Locate every blood parasite and identify its species.
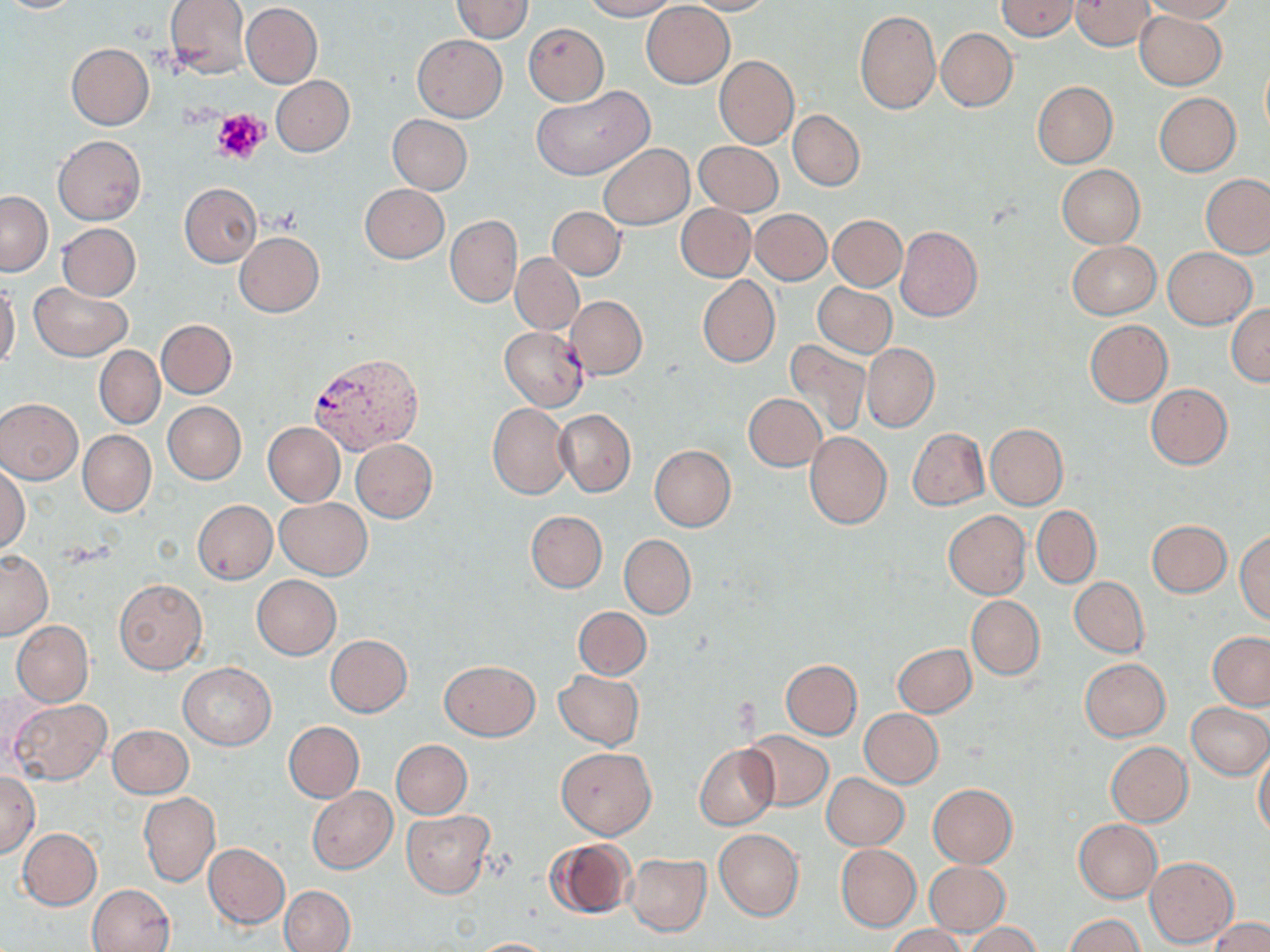
Approximate bounding boxes as (x1,y1)-(x2,y2) corner pairs in pixels.
Plasmodium vivax-infected red blood cells: (311,353)-(424,455).
No Plasmodium falciparum, Plasmodium ovale, Plasmodium malariae, Babesia divergens, or Trypanosoma brucei observed.

slide-level diagnosis = Plasmodium vivax
stain = May-Grünwald-Giemsa
image size = 1270×952 pixels
uninfected red blood cell locations = approximate bounding boxes as (x1,y1)-(x2,y2) corner pairs in pixels: (0,0)-(84,14), (164,0)-(251,79), (449,0)-(535,42), (581,0)-(677,21), (677,0)-(776,15), (997,0)-(1079,40), (1069,0)-(1155,50), (1137,0)-(1238,22), (642,2)-(734,88), (241,3)-(322,87), (855,10)-(940,113), (1134,10)-(1225,90), (523,22)-(609,106), (938,27)-(1017,111), (413,35)-(508,121), (65,43)-(155,130), (714,55)-(800,148), (1260,59)-(1270,139), (271,75)-(354,155), (1032,81)-(1117,167), (532,85)-(654,180), (1154,93)-(1241,175), (788,111)-(865,191), (388,115)-(473,194), (53,136)-(146,224), (693,141)-(783,215), (599,144)-(693,230), (1057,164)-(1144,248), (1200,174)-(1270,258), (179,183)-(262,268), (360,184)-(450,262), (0,191)-(52,275), (676,204)-(755,281), (548,207)-(625,279), (749,209)-(831,285), (446,215)-(521,307), (829,215)-(906,290), (57,223)-(140,301), (896,225)-(982,321), (236,232)-(324,317), (1067,241)-(1160,319), (1163,248)-(1255,329), (511,253)-(583,334), (697,276)-(779,367), (0,282)-(20,372), (813,282)-(896,358), (30,283)-(133,361), (567,296)-(647,379), (1227,304)-(1270,385), (155,319)-(236,398), (1085,320)-(1172,406), (500,327)-(588,409), (785,340)-(871,437), (862,342)-(939,432), (94,345)-(165,429), (1146,384)-(1233,469), (743,393)-(826,471), (0,398)-(82,483), (163,402)-(246,483), (488,402)-(574,499), (554,408)-(636,497), (263,422)-(344,507), (986,423)-(1068,509), (907,428)-(989,510), (78,430)-(156,516), (805,432)-(891,528), (351,439)-(436,522), (650,445)-(735,531), (0,464)-(29,554), (276,497)-(371,579), (193,500)-(277,583), (1031,506)-(1101,588), (526,511)-(607,592), (943,511)-(1031,599), (1147,520)-(1231,597), (1236,530)-(1270,625), (620,534)-(696,618), (0,549)-(53,639), (252,575)-(342,660), (1070,577)-(1149,657), (114,579)-(207,674), (966,596)-(1044,680), (574,606)-(651,680), (12,621)-(93,705), (1208,632)-(1270,709), (326,635)-(412,717), (893,643)-(976,717), (1080,658)-(1170,740), (440,660)-(539,740), (780,660)-(862,739), (178,663)-(276,750), (554,669)-(643,750), (9,698)-(112,785), (1186,703)-(1270,777), (860,709)-(943,787), (283,722)-(364,803), (107,725)-(193,798), (742,731)-(834,811), (392,740)-(472,818), (1106,742)-(1193,826), (694,744)-(778,830), (556,746)-(656,838), (1253,750)-(1270,838), (1,772)-(40,858), (821,774)-(908,850), (928,783)-(1017,867), (307,786)-(397,874), (139,793)-(220,886), (401,810)-(495,897), (1073,819)-(1161,903), (18,829)-(102,909), (714,830)-(804,921), (544,837)-(634,920), (203,843)-(290,928), (837,845)-(920,931), (625,853)-(711,936), (1146,857)-(1238,947), (924,861)-(1010,936), (87,883)-(175,952), (280,885)-(355,952), (1067,914)-(1145,951), (1209,917)-(1270,952), (965,924)-(1042,952), (888,925)-(967,952), (468,937)-(562,951)
field of view = one of a larger specimen
preparation = thin blood film
platelet locations = approximate bounding boxes as (x1,y1)-(x2,y2) corner pairs in pixels: (212,108)-(269,165)
modality = light microscopy
magnification = 1000x